Report the malaria status of this cell.
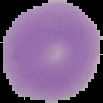

It is uninfected.

From a thin blood smear. Segmented cell region on a black background. Image is 103×103 pixels.